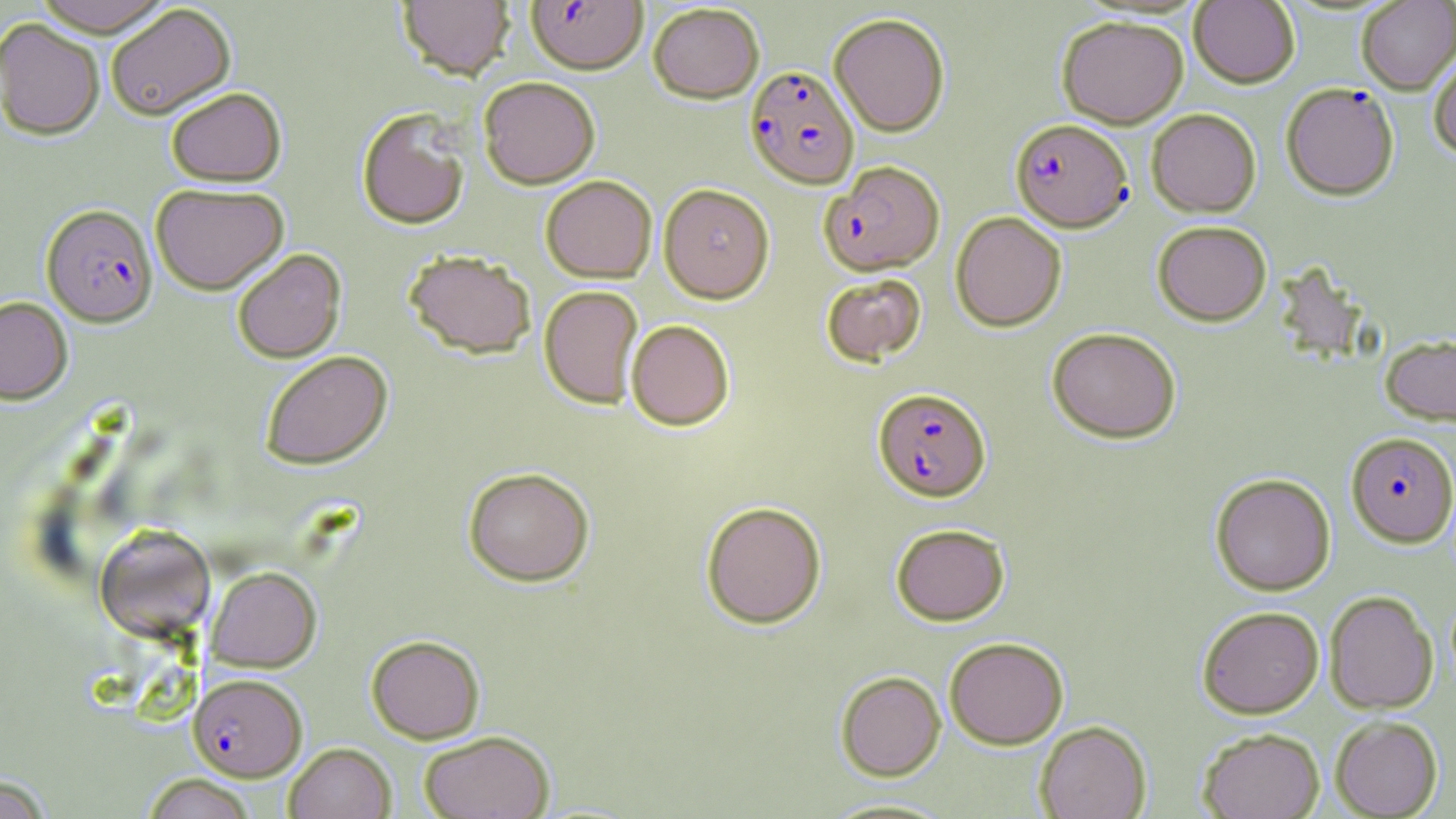
slide-level diagnosis = Plasmodium falciparum
magnification = 1000x
image size = 1456×819 pixels
modality = light microscopy
stain = May-Grünwald-Giemsa
field of view = single
Plasmodium falciparum-infected red blood cell locations = approximate bounding boxes as named x1/y1/x2/y2 corners in pixels: (x1=526, y1=0, x2=648, y2=74), (x1=744, y1=66, x2=858, y2=189), (x1=1282, y1=83, x2=1399, y2=200), (x1=1011, y1=118, x2=1132, y2=232), (x1=821, y1=161, x2=946, y2=275), (x1=42, y1=203, x2=157, y2=326), (x1=873, y1=387, x2=991, y2=501), (x1=1346, y1=432, x2=1456, y2=546), (x1=188, y1=673, x2=307, y2=781)
uninfected red blood cell locations = approximate bounding boxes as named x1/y1/x2/y2 corners in pixels: (x1=33, y1=0, x2=173, y2=36), (x1=397, y1=0, x2=515, y2=80), (x1=1356, y1=0, x2=1456, y2=93), (x1=1189, y1=1, x2=1300, y2=88), (x1=648, y1=3, x2=764, y2=103), (x1=105, y1=4, x2=236, y2=120), (x1=828, y1=12, x2=950, y2=136), (x1=1057, y1=15, x2=1188, y2=128), (x1=0, y1=18, x2=105, y2=140), (x1=1428, y1=50, x2=1456, y2=158), (x1=478, y1=76, x2=601, y2=188), (x1=166, y1=86, x2=286, y2=186), (x1=356, y1=108, x2=471, y2=229), (x1=1147, y1=108, x2=1261, y2=217), (x1=540, y1=175, x2=657, y2=283), (x1=151, y1=182, x2=289, y2=294), (x1=658, y1=183, x2=774, y2=303), (x1=950, y1=211, x2=1067, y2=332), (x1=1152, y1=220, x2=1272, y2=326), (x1=232, y1=249, x2=346, y2=362), (x1=403, y1=249, x2=536, y2=359), (x1=821, y1=273, x2=926, y2=365), (x1=539, y1=285, x2=643, y2=408), (x1=0, y1=296, x2=73, y2=403), (x1=626, y1=319, x2=735, y2=430), (x1=1046, y1=326, x2=1181, y2=443), (x1=1380, y1=335, x2=1456, y2=426), (x1=260, y1=350, x2=393, y2=469), (x1=463, y1=466, x2=594, y2=586), (x1=1210, y1=472, x2=1335, y2=596), (x1=701, y1=500, x2=826, y2=628), (x1=891, y1=523, x2=1010, y2=626), (x1=94, y1=524, x2=216, y2=641), (x1=206, y1=566, x2=321, y2=672), (x1=1324, y1=590, x2=1438, y2=714), (x1=1197, y1=605, x2=1324, y2=718), (x1=366, y1=635, x2=485, y2=743), (x1=944, y1=637, x2=1069, y2=749), (x1=835, y1=671, x2=946, y2=781), (x1=1330, y1=715, x2=1443, y2=818), (x1=1035, y1=721, x2=1151, y2=819), (x1=1198, y1=727, x2=1325, y2=819), (x1=418, y1=730, x2=555, y2=819), (x1=284, y1=742, x2=396, y2=819), (x1=0, y1=774, x2=54, y2=819), (x1=141, y1=774, x2=257, y2=819), (x1=816, y1=797, x2=962, y2=818)
preparation = thin blood film